Locate and identify every blood parasite.
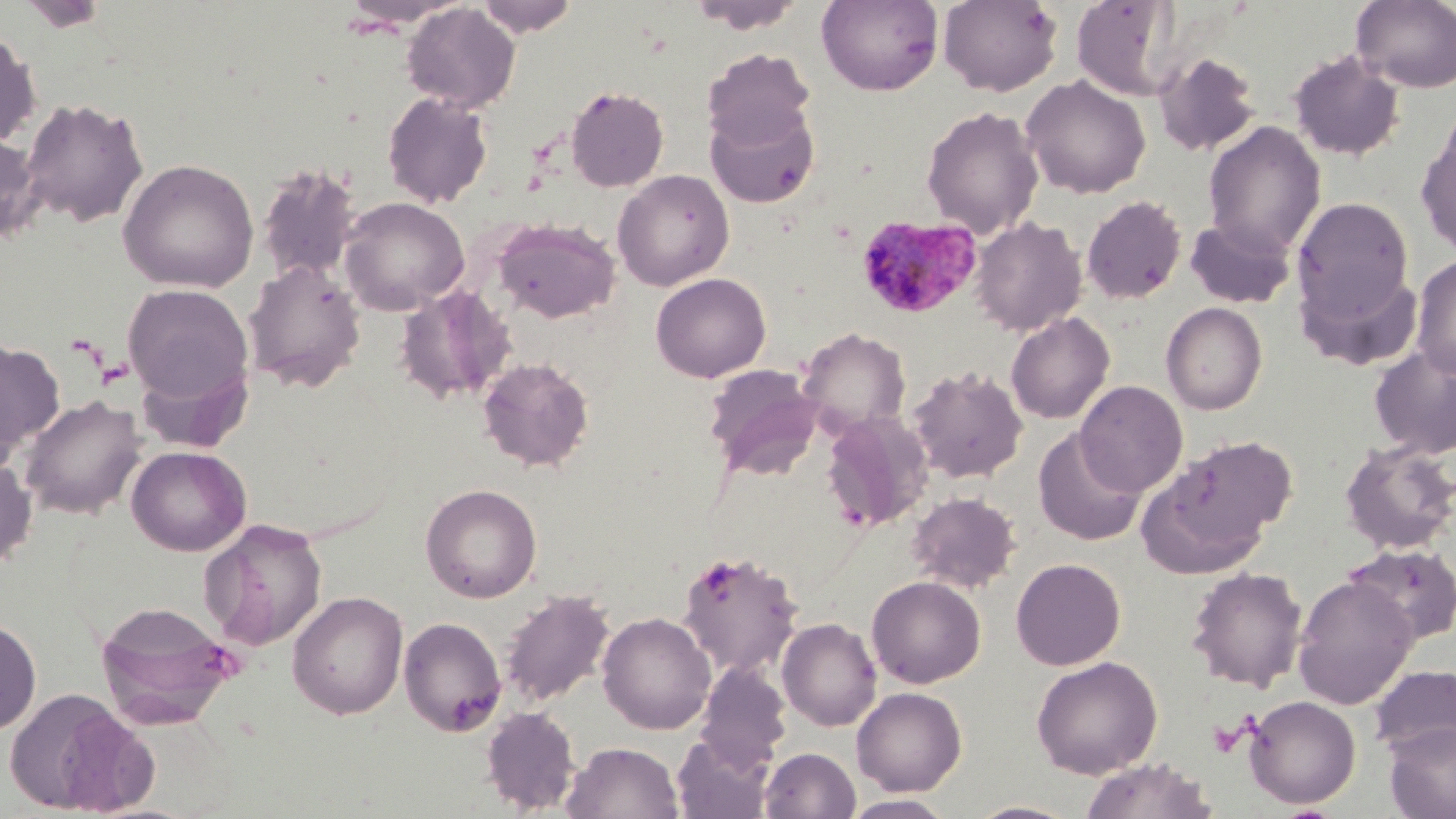
Approximate bounding boxes as (x1,y1)-(x2,y2) corner pairs in pixels.
Plasmodium malariae-infected red blood cells: (856,214)-(983,321).
No Plasmodium falciparum, Plasmodium ovale, Plasmodium vivax, Babesia divergens, or Trypanosoma brucei observed.

Uninfected red blood cell locations: (16,0)-(111,31), (339,0)-(469,29), (474,0)-(579,37), (687,0)-(806,34), (816,0)-(943,95), (938,0)-(1062,96), (1071,0)-(1183,101), (1351,0)-(1456,93), (402,3)-(520,113), (0,31)-(41,147), (702,48)-(816,150), (1288,50)-(1406,161), (1153,51)-(1262,157), (1021,75)-(1151,199), (566,86)-(669,192), (382,91)-(494,209), (20,96)-(149,229), (706,104)-(818,208), (921,105)-(1044,239), (1203,122)-(1326,258), (1416,128)-(1456,259), (0,134)-(44,243), (117,158)-(259,292), (256,164)-(360,285), (612,170)-(734,291), (1081,195)-(1186,304), (339,196)-(469,316), (1292,197)-(1415,323), (971,216)-(1087,336), (1185,216)-(1295,308), (493,217)-(621,324), (1410,256)-(1456,379), (244,259)-(365,392), (650,272)-(771,382), (122,283)-(253,407), (395,285)-(515,405), (1161,302)-(1267,415), (1005,312)-(1115,425), (797,327)-(911,436), (0,340)-(65,458), (1369,345)-(1456,460), (478,356)-(594,471), (703,364)-(821,479), (908,365)-(1029,484), (1075,380)-(1188,497), (18,394)-(146,519), (821,411)-(933,530), (1033,429)-(1146,546), (1142,435)-(1294,570), (1339,441)-(1456,556), (126,445)-(251,556), (0,456)-(37,573), (420,483)-(542,603), (906,491)-(1022,593), (200,518)-(328,652), (1344,544)-(1456,646), (677,548)-(804,679), (1010,558)-(1126,670), (1185,567)-(1309,692), (1293,575)-(1417,707), (866,576)-(986,688), (499,589)-(615,708), (287,590)-(409,719), (95,599)-(242,729), (597,612)-(716,734), (398,616)-(507,736), (777,617)-(881,731), (0,618)-(41,737), (1031,655)-(1162,778), (695,661)-(792,772), (1369,664)-(1456,760), (3,686)-(143,815), (851,687)-(967,796), (1244,695)-(1362,808), (481,707)-(581,814), (1385,722)-(1456,819), (672,731)-(775,819), (562,741)-(683,819), (759,747)-(861,819), (1078,757)-(1217,819), (841,795)-(957,818), (966,800)-(1082,819). Slide-level diagnosis: Plasmodium malariae. Single field of view. Thin blood smear. Image is 1456×819 pixels. Optical microscopy. May-Grünwald-Giemsa stain. Captured at 1000x magnification.